Comment on the morphology of the red blood cells.
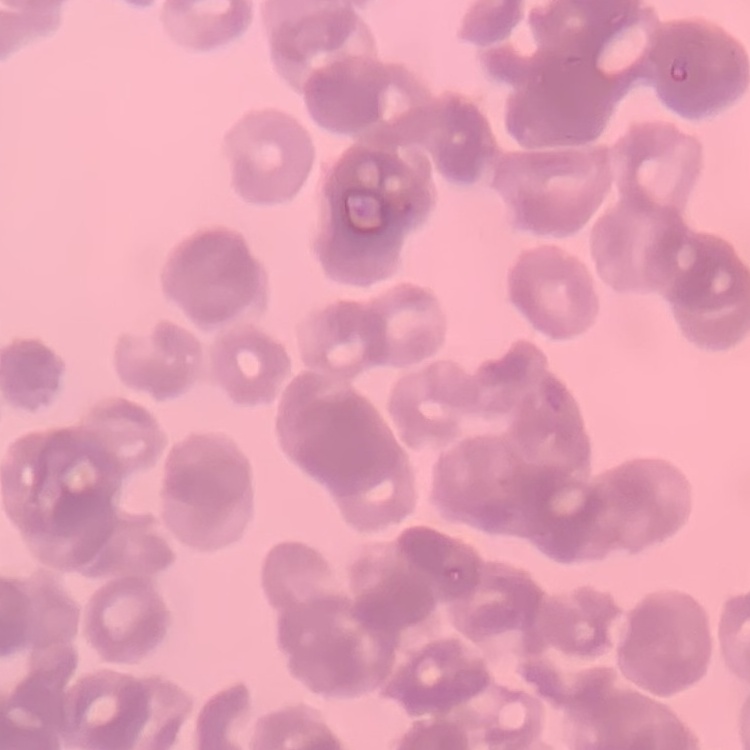

Rouleaux formation.

Square crop of a larger photomicrograph. Thin blood film. Field's or Giemsa stain.